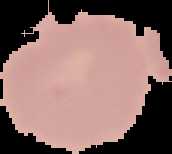

malaria status = uninfected
preparation = thin blood smear
image type = cell region segmented out of the field of view; surrounding area masked to black
image size = 172×154 pixels